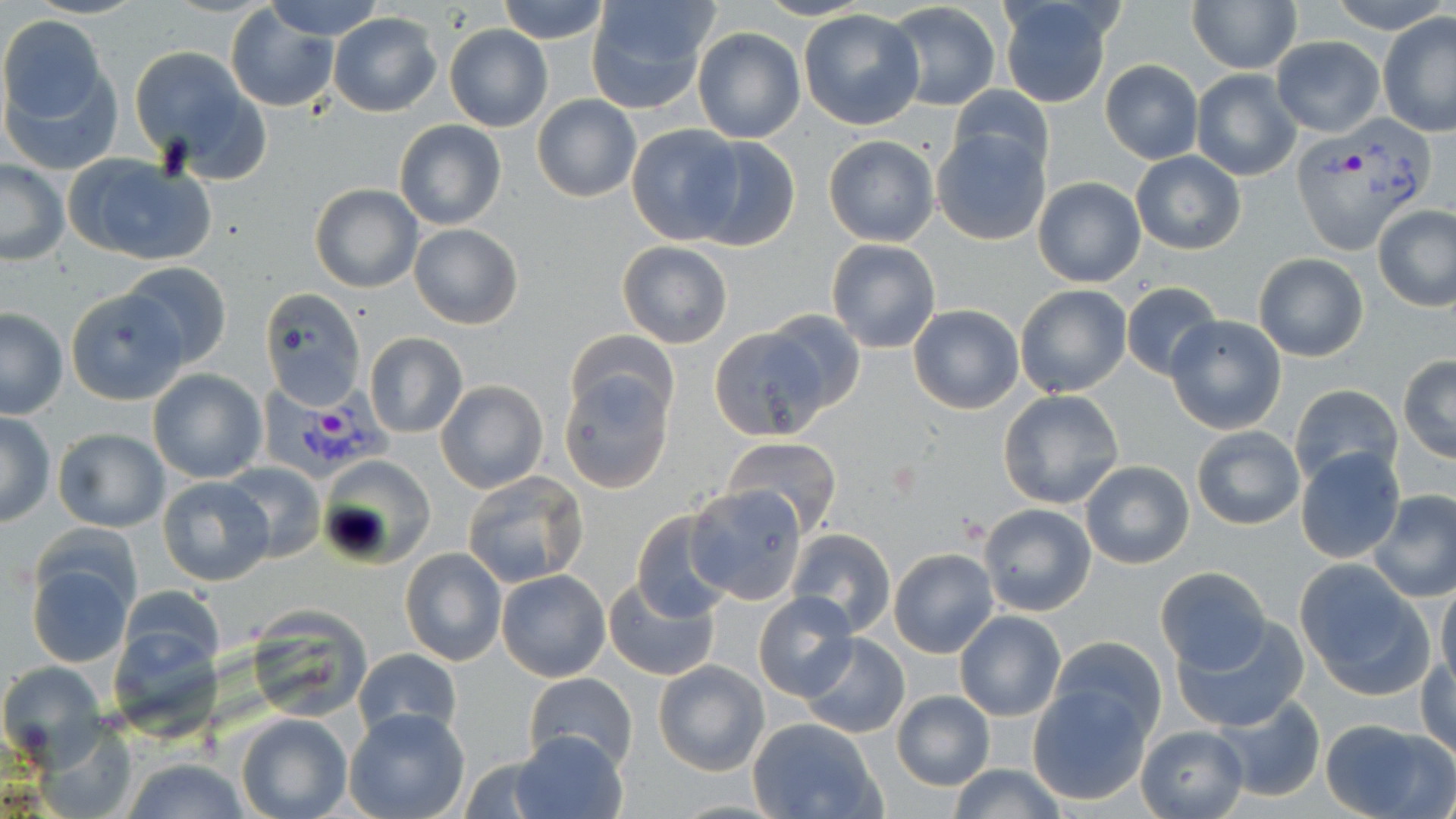

{
  "slide_level_diagnosis": "Plasmodium vivax",
  "magnification": "1000x",
  "stain": "May-Grünwald-Giemsa",
  "preparation": "thin blood film",
  "plasmodium_vivax_infected_red_blood_cell_locations": "approximate bounding boxes as (x1,y1)-(x2,y2) corner pairs in pixels: (1293,117)-(1430,252), (256,381)-(397,488)",
  "uninfected_red_blood_cell_locations": "approximate bounding boxes as (x1,y1)-(x2,y2) corner pairs in pixels: (25,0)-(145,19), (266,0)-(383,40), (495,0)-(612,45), (584,0)-(718,114), (1187,0)-(1302,74), (1334,0)-(1445,30), (996,1)-(1117,109), (883,2)-(1002,112), (225,5)-(340,112), (798,10)-(926,130), (329,11)-(441,118), (0,13)-(116,152), (1379,13)-(1456,136), (444,24)-(551,132), (693,27)-(805,143), (1271,37)-(1384,135), (130,45)-(262,171), (1100,59)-(1203,164), (1190,68)-(1302,180), (948,86)-(1053,178), (533,94)-(641,202), (393,120)-(506,230), (626,124)-(741,244), (931,127)-(1050,246), (823,135)-(941,248), (688,137)-(800,250), (1130,150)-(1246,254), (64,154)-(216,267), (0,159)-(70,266), (1032,175)-(1147,288), (310,184)-(424,293), (1372,204)-(1456,311), (408,223)-(523,329), (826,238)-(941,353), (617,240)-(733,349), (1254,253)-(1368,361), (118,262)-(232,370), (1120,281)-(1224,382), (1015,284)-(1132,398), (67,289)-(188,406), (261,292)-(367,410), (909,304)-(1025,414), (0,308)-(68,419), (763,309)-(865,415), (1165,315)-(1288,433), (714,321)-(845,437), (566,330)-(678,425), (364,332)-(468,439), (1398,357)-(1456,462), (148,368)-(267,483), (557,374)-(674,493), (436,380)-(549,494), (1290,383)-(1403,487), (997,389)-(1126,510), (1,411)-(55,527), (1191,426)-(1304,529), (53,428)-(171,532), (723,435)-(842,535), (1294,447)-(1405,562), (318,457)-(434,568), (1080,460)-(1194,568), (220,461)-(325,563), (462,470)-(591,588), (155,475)-(277,587), (686,484)-(808,604), (1369,490)-(1456,602), (979,503)-(1097,615), (630,511)-(734,623), (787,528)-(896,636), (401,548)-(506,666), (888,548)-(999,659), (24,554)-(136,667), (1295,560)-(1431,695), (1154,566)-(1271,674), (497,569)-(610,681), (603,574)-(720,680), (1434,581)-(1456,691), (753,593)-(858,701), (248,606)-(377,724), (954,611)-(1067,722), (1175,618)-(1312,732), (800,634)-(909,739), (1053,636)-(1166,737), (353,647)-(461,744), (1418,655)-(1455,760), (653,659)-(769,775), (0,661)-(107,763), (522,673)-(638,771), (1027,684)-(1152,805), (891,689)-(997,792), (1208,693)-(1326,803), (344,707)-(471,819), (235,711)-(353,819), (1318,716)-(1454,819), (748,718)-(883,819), (1135,724)-(1249,818), (509,729)-(626,818), (118,757)-(254,819), (945,764)-(1067,819)",
  "field_of_view": "single",
  "modality": "optical microscopy",
  "image_size": "1456×819 pixels"
}